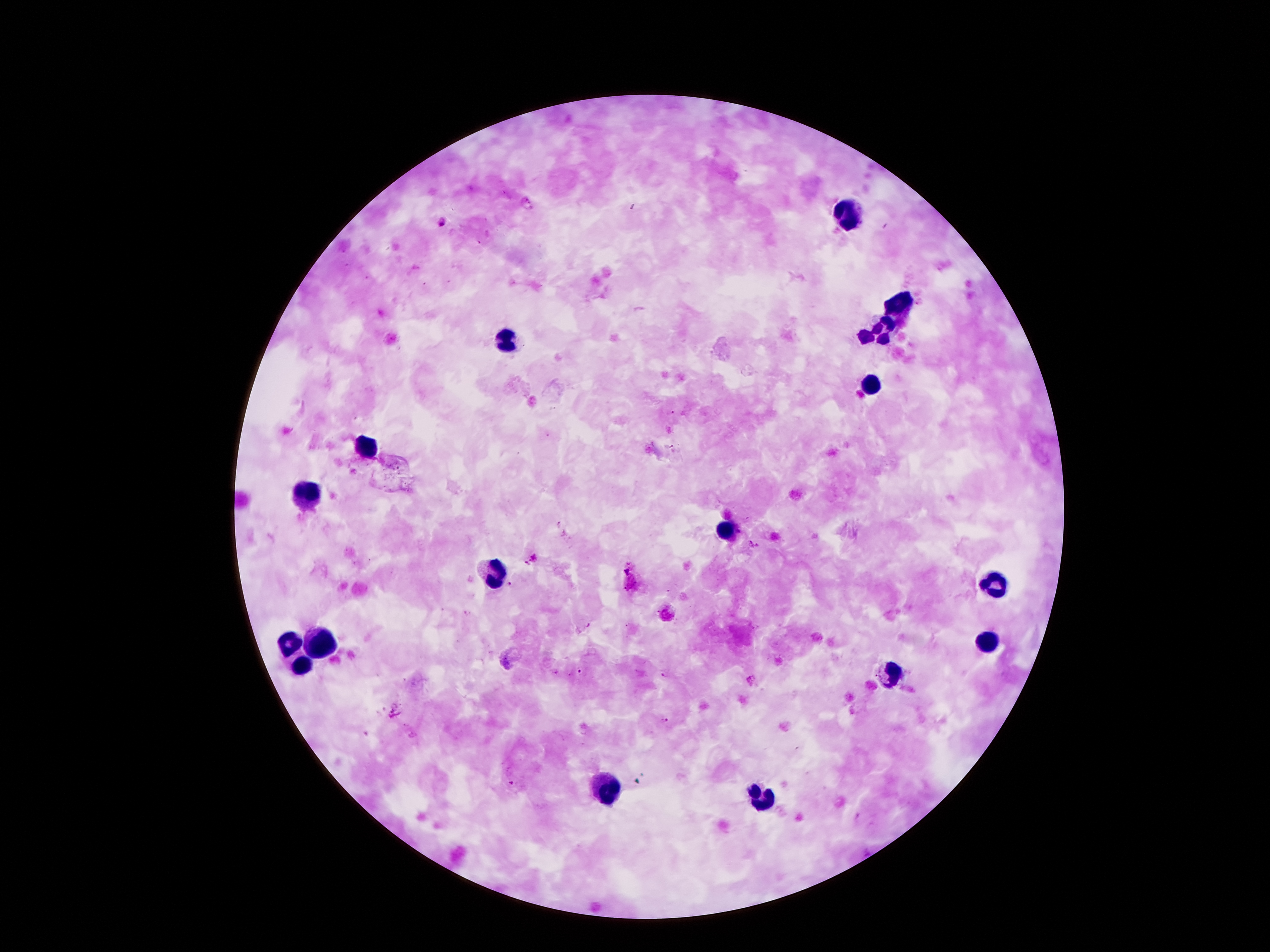

Approximate centers as (x, y) in pixels.
Summary:
  - Leukocyte locations: (844, 214), (897, 304), (889, 322), (880, 333), (864, 335), (505, 337), (871, 383), (364, 444), (302, 494), (727, 532), (490, 571), (992, 584), (316, 640), (990, 642), (288, 644), (299, 666), (893, 672), (604, 789), (755, 797)
  - Plasmodium parasite locations: (441, 222), (750, 545), (760, 545), (535, 557), (525, 565), (509, 583), (581, 671), (667, 674), (666, 721), (510, 784)
  - Patient malaria status: infected with Plasmodium falciparum
  - Capture: smartphone through the microscope eyepiece
  - Stain: Giemsa
  - Image size: 1270×952 pixels
  - Preparation: thick blood smear
  - Field of view: one from this slide
  - Magnification: 100x